Assess this cell for malaria.
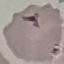
It is uninfected.

Giemsa-stained preparation. Automatically extracted cell patch, resized to 64 × 64 pixels. Acquired by smartphone through the microscope eyepiece. Thin blood film.